Classify this cell by malaria status.
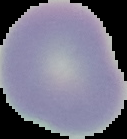

It is uninfected.

Summary:
  - Image size: 127×139 pixels
  - Preparation: thin blood film
  - Image type: segmented cell region on a black background